Point out each Plasmodium parasite.
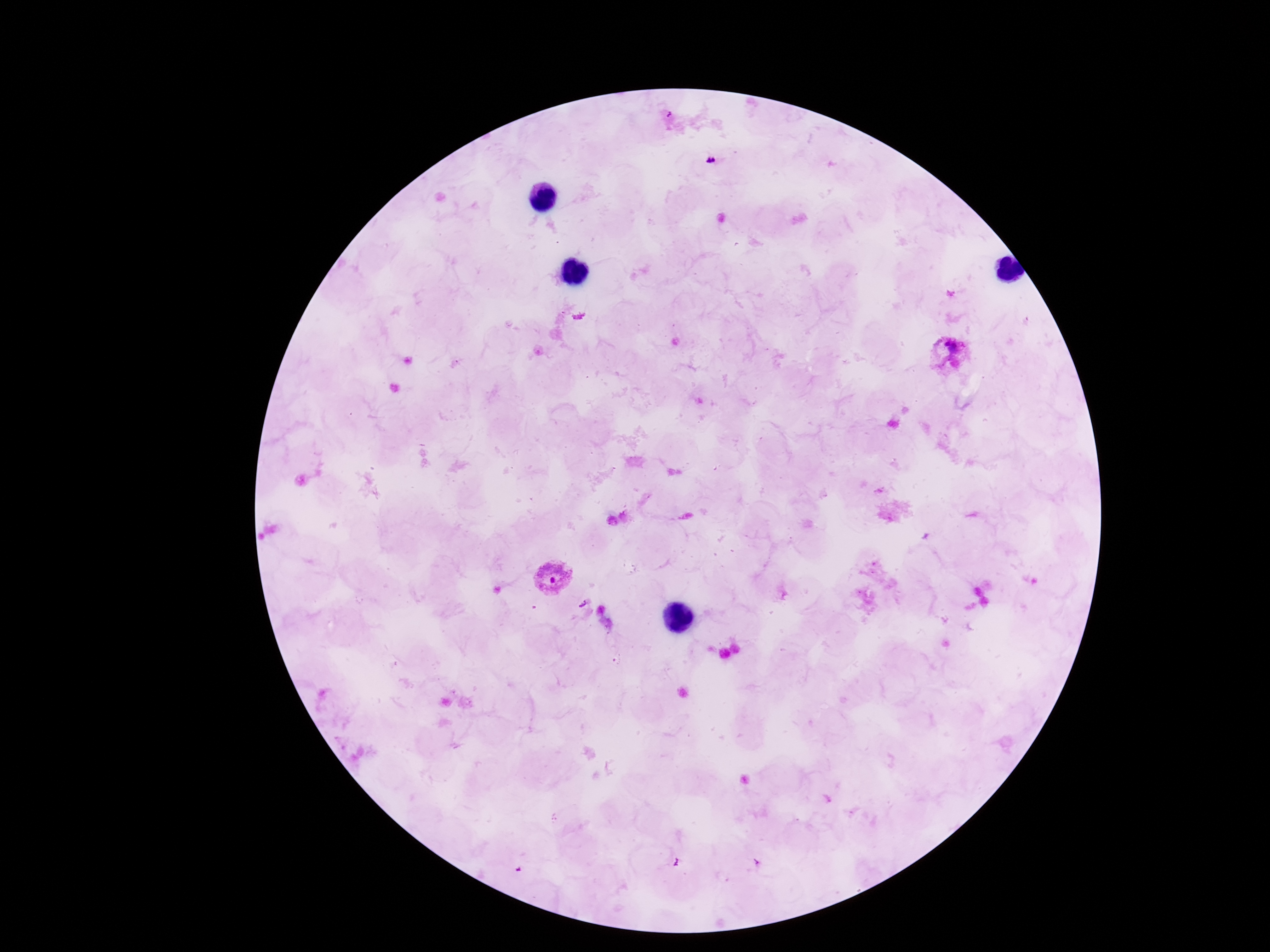
Approximate object centers, in pixels from the top-left corner.
Plasmodium parasites: (x=711, y=160), (x=952, y=353), (x=552, y=578).

Image is 1270×952 pixels. Patient malaria status: infected. 100x magnification. Thick blood film. Single field of view. Giemsa stain. Smartphone photograph taken through the microscope eyepiece.